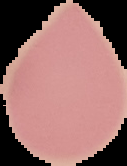
Summary:
  - Preparation: thin blood film
  - Image size: 127×166 pixels
  - Result: no malaria parasites seen
  - Image type: segmented cell region on a black background